Point out each Plasmodium parasite.
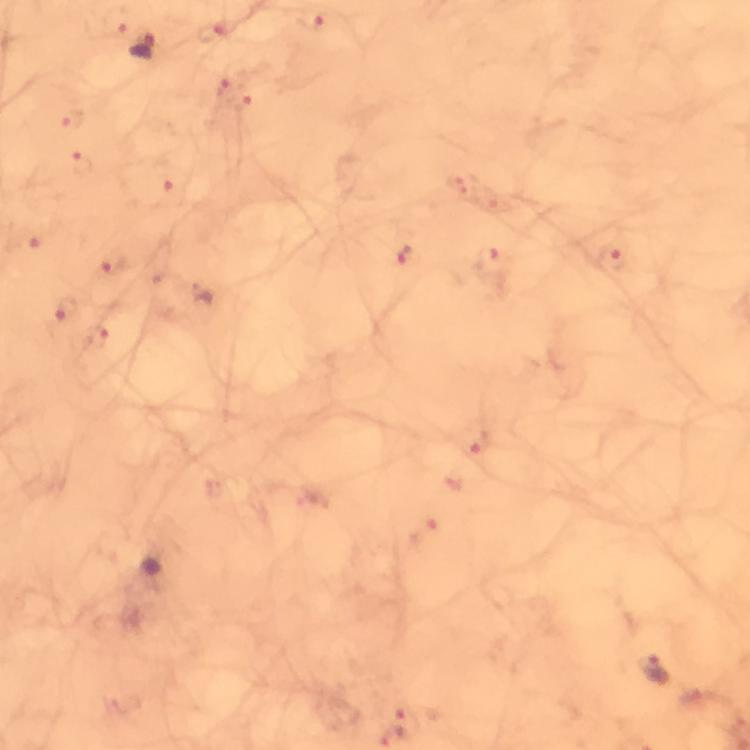
Approximate object centers, in pixels from the top-left corner.
Plasmodium parasites: (x=145, y=46), (x=657, y=673).

From a diagnostic examination for malaria. Immersion oil was used. Giemsa stain. 100x magnification. Photographed with a smartphone mounted on the microscope. Cropped region of a single field of view. Thick blood film. Image is 750×750 pixels.